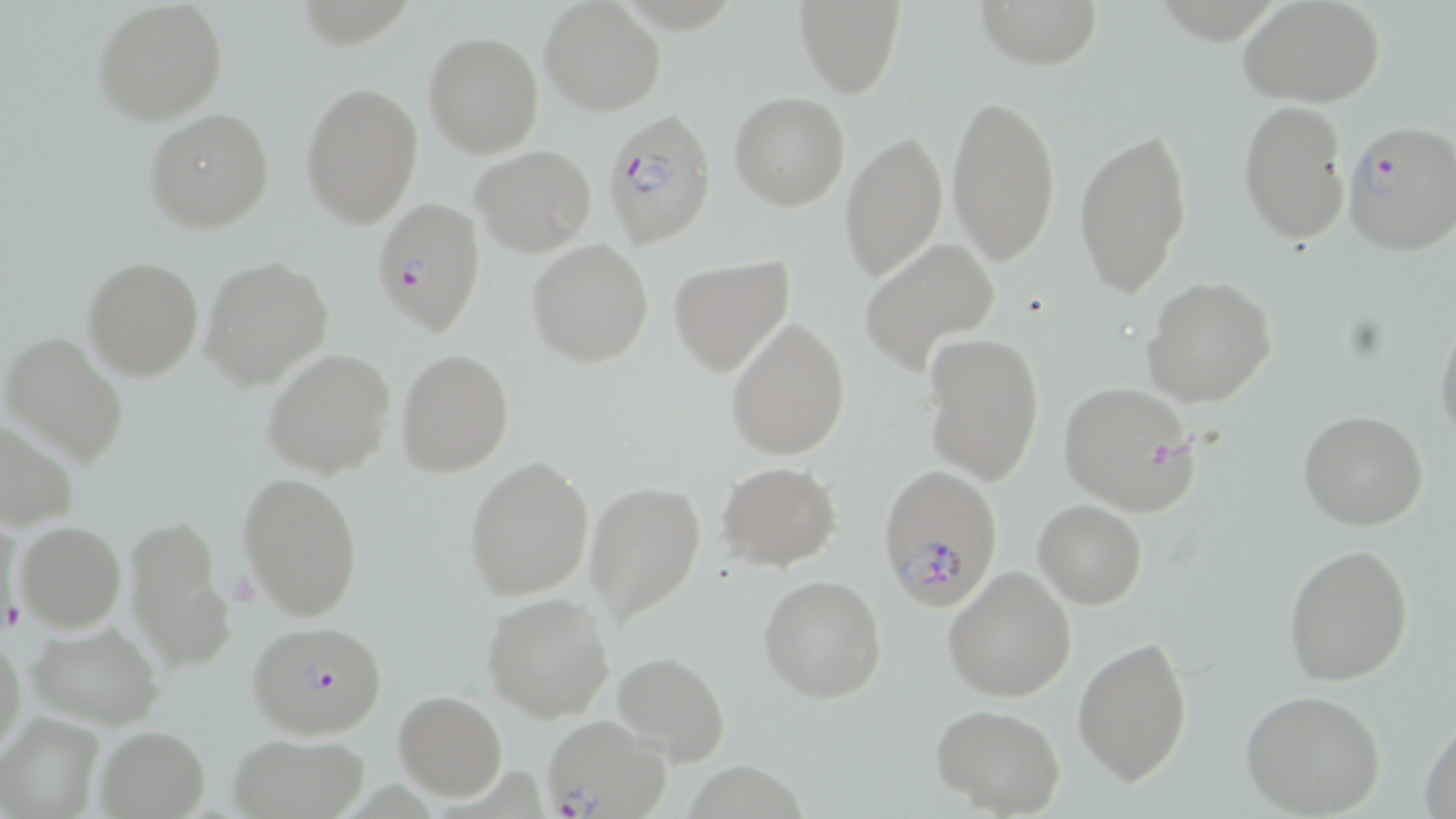

slide_level_diagnosis: Plasmodium falciparum
magnification: 1000x
plasmodium_falciparum_infected_red_blood_cell_locations: 'approximate bounding boxes as named x1/y1/x2/y2 corners in pixels: (x1=605, y1=109, x2=717, y2=245), (x1=1340, y1=121, x2=1456, y2=258), (x1=373, y1=199, x2=485, y2=340), (x1=881, y1=465, x2=1002, y2=610), (x1=248, y1=621, x2=390, y2=739), (x1=541, y1=715, x2=673, y2=819)'
image_size: 1456×819 pixels
platelet_locations: 'approximate bounding boxes as named x1/y1/x2/y2 corners in pixels: (x1=3, y1=597, x2=26, y2=630)'
uninfected_red_blood_cell_locations: 'approximate bounding boxes as named x1/y1/x2/y2 corners in pixels: (x1=91, y1=0, x2=228, y2=125), (x1=794, y1=0, x2=904, y2=97), (x1=974, y1=0, x2=1104, y2=69), (x1=1240, y1=1, x2=1386, y2=108), (x1=540, y1=2, x2=663, y2=116), (x1=423, y1=31, x2=543, y2=158), (x1=299, y1=83, x2=423, y2=227), (x1=729, y1=92, x2=849, y2=210), (x1=945, y1=93, x2=1062, y2=265), (x1=1237, y1=100, x2=1351, y2=246), (x1=142, y1=108, x2=274, y2=233), (x1=1073, y1=124, x2=1194, y2=300), (x1=840, y1=131, x2=946, y2=282), (x1=472, y1=146, x2=596, y2=257), (x1=527, y1=239, x2=654, y2=368), (x1=860, y1=239, x2=998, y2=374), (x1=668, y1=255, x2=795, y2=377), (x1=82, y1=256, x2=204, y2=381), (x1=203, y1=256, x2=332, y2=389), (x1=1141, y1=276, x2=1277, y2=409), (x1=1433, y1=313, x2=1456, y2=444), (x1=724, y1=318, x2=851, y2=460), (x1=1, y1=332, x2=129, y2=467), (x1=921, y1=332, x2=1044, y2=485), (x1=263, y1=347, x2=395, y2=479), (x1=397, y1=348, x2=514, y2=476), (x1=1057, y1=381, x2=1200, y2=515), (x1=1299, y1=411, x2=1427, y2=530), (x1=1, y1=415, x2=80, y2=530), (x1=464, y1=455, x2=594, y2=600), (x1=717, y1=462, x2=841, y2=569), (x1=238, y1=469, x2=363, y2=620), (x1=584, y1=480, x2=706, y2=625), (x1=1033, y1=499, x2=1148, y2=608), (x1=126, y1=513, x2=235, y2=674), (x1=2, y1=518, x2=27, y2=638), (x1=13, y1=521, x2=126, y2=632), (x1=1283, y1=542, x2=1414, y2=687), (x1=942, y1=566, x2=1078, y2=702), (x1=759, y1=574, x2=888, y2=704), (x1=483, y1=593, x2=614, y2=723), (x1=27, y1=621, x2=164, y2=730), (x1=0, y1=628, x2=25, y2=764), (x1=1073, y1=634, x2=1194, y2=787), (x1=611, y1=650, x2=729, y2=766), (x1=1239, y1=688, x2=1387, y2=817), (x1=393, y1=690, x2=507, y2=801), (x1=934, y1=705, x2=1066, y2=816), (x1=0, y1=712, x2=105, y2=819), (x1=1420, y1=714, x2=1456, y2=818), (x1=95, y1=726, x2=210, y2=818), (x1=225, y1=734, x2=372, y2=819)'
stain: May-Grünwald-Giemsa
field_of_view: one of a larger specimen
preparation: thin blood film
modality: optical microscopy